Assess the morphology of the red blood cells.
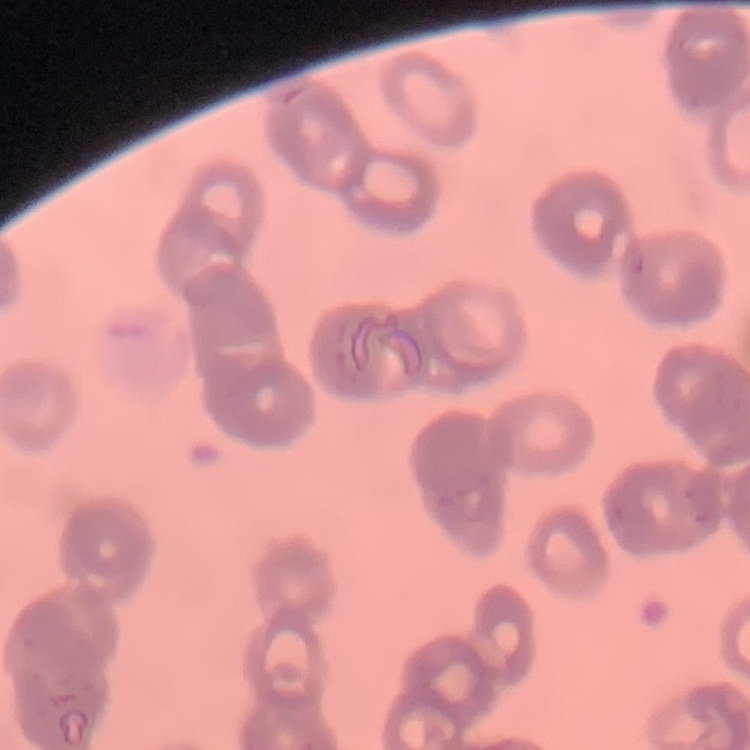

They show rouleaux formation.

Summary:
  - Image type: square crop of a larger photomicrograph
  - Stain: Field's or Giemsa
  - Preparation: thin blood film